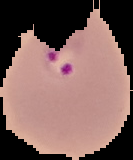

Summary:
  - Image size: 133×160 pixels
  - Preparation: thin blood smear
  - Image type: segmented cell region with the area outside set to black
  - Malaria status: parasitized